Name the parasite shown.
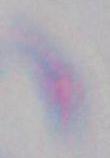
Toxoplasma gondii.

Summary:
  - Magnification: 1000x
  - Modality: micrograph